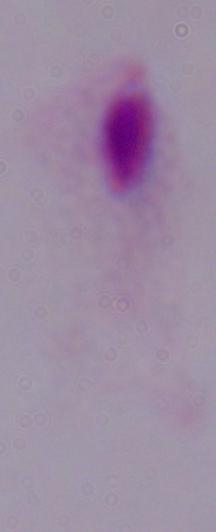 A trichomonad is shown. 1000x magnification. Photomicrograph.